Classify this cell by malaria status.
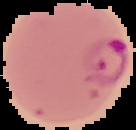

Parasitized.

Summary:
  - Preparation: thin blood smear
  - Image size: 136×130 pixels
  - Image type: segmented cell region on a black background